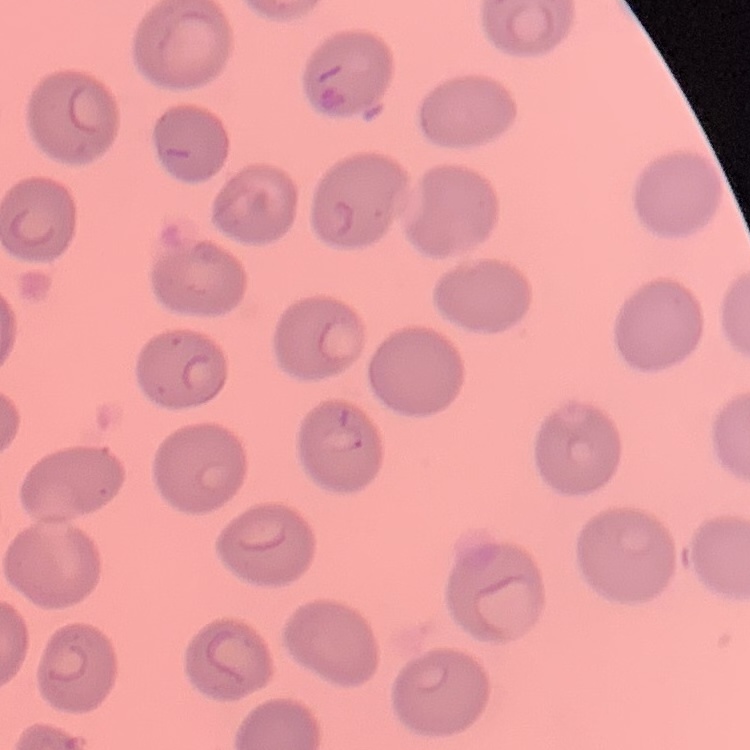
The erythrocytes show no rouleaux formation. One tile cut from a larger photomicrograph. Stained with either Field's or Giemsa. Thin blood smear.